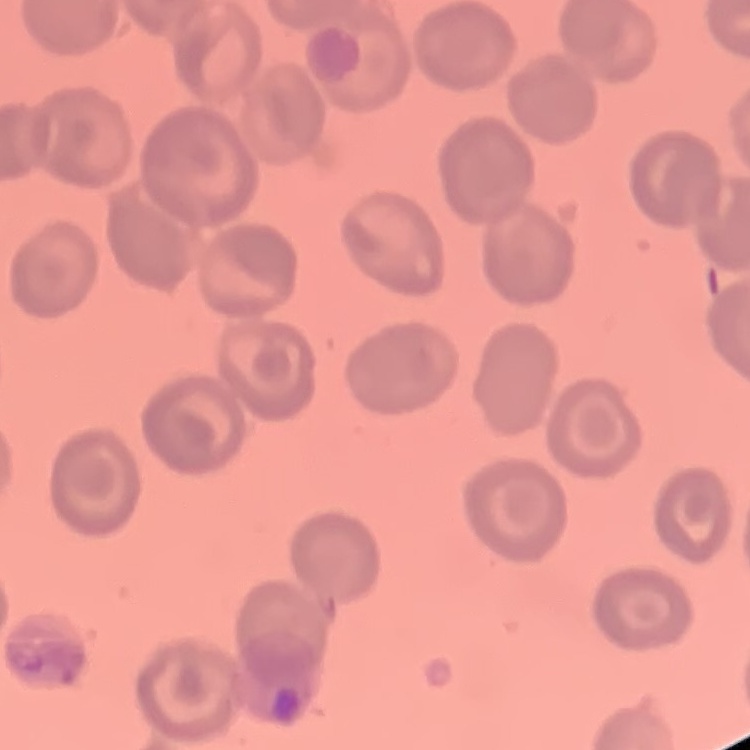
erythrocyte_morphology: no rouleaux formation
image_type: square crop of a larger photomicrograph
stain: Field's or Giemsa
preparation: thin blood film